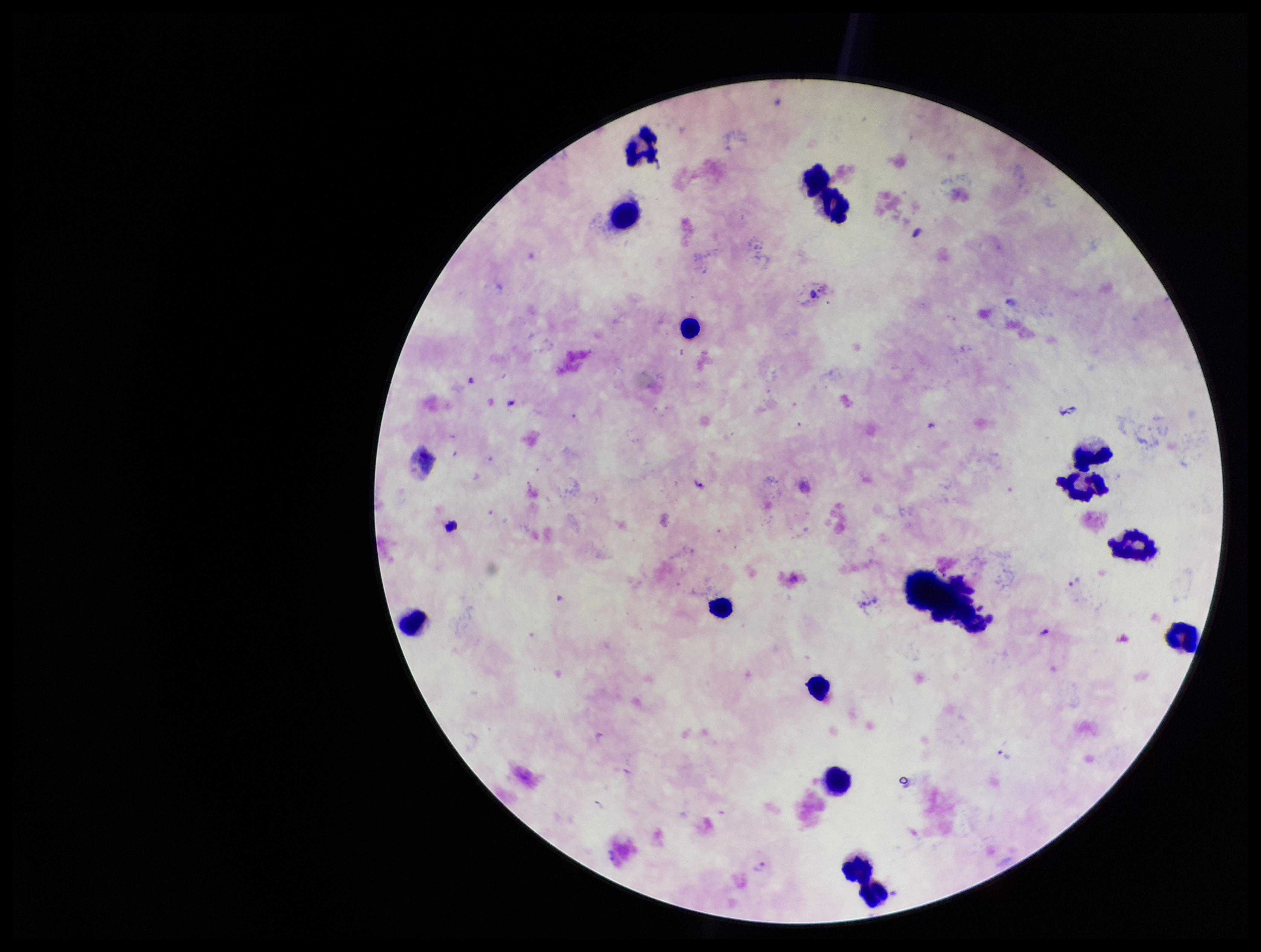
Species reported for this patient: Plasmodium vivax. Patient malaria status: positive. Image is 1261×952 pixels. Preparation: thick smear. Single field of view. Parasite count: 1. Photographed through the microscope eyepiece with a smartphone camera. Stained with Giemsa. Leukocyte count: 15. Plasmodium parasites: detected.